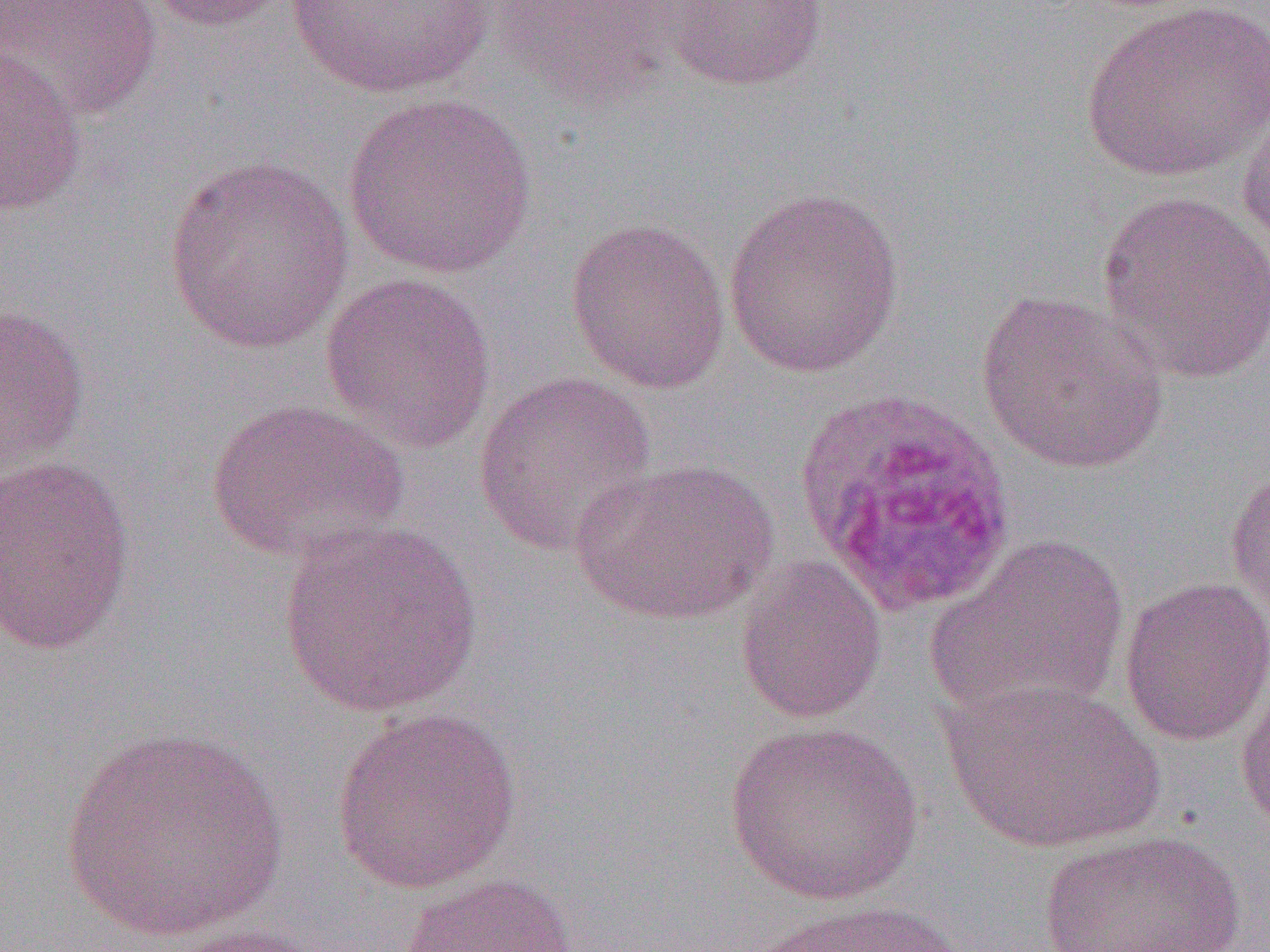

slide_level_diagnosis: Plasmodium ovale
magnification: 1000x
modality: optical microscopy
preparation: thin blood smear
field_of_view: one of a larger specimen
image_size: 1270×952 pixels
plasmodium_ovale_infected_red_blood_cell_locations: 'approximate bounding boxes as (x1, y1, x2, y2) in pixels: (793, 385, 1017, 617)'
uninfected_red_blood_cell_locations: 'approximate bounding boxes as (x1, y1, x2, y2) in pixels: (0, 0, 164, 120), (141, 0, 298, 33), (278, 0, 506, 102), (491, 0, 666, 111), (660, 0, 829, 91), (1082, 0, 1270, 184), (0, 46, 88, 217), (1236, 89, 1270, 254), (341, 91, 538, 280), (164, 155, 355, 356), (722, 185, 905, 380), (1096, 191, 1270, 384), (565, 217, 732, 394), (320, 271, 497, 453), (975, 289, 1169, 475), (0, 304, 91, 475), (473, 371, 657, 557), (206, 395, 411, 565), (0, 453, 137, 655), (570, 456, 780, 627), (1225, 466, 1270, 620), (278, 518, 483, 718), (926, 534, 1130, 725), (734, 555, 888, 725), (1118, 576, 1270, 746), (1235, 675, 1270, 834), (941, 677, 1163, 854), (329, 705, 523, 894), (724, 720, 925, 906), (59, 726, 290, 945), (1035, 830, 1249, 951), (396, 871, 580, 952), (744, 898, 973, 952), (160, 922, 340, 952)'